Locate and identify every blood parasite.
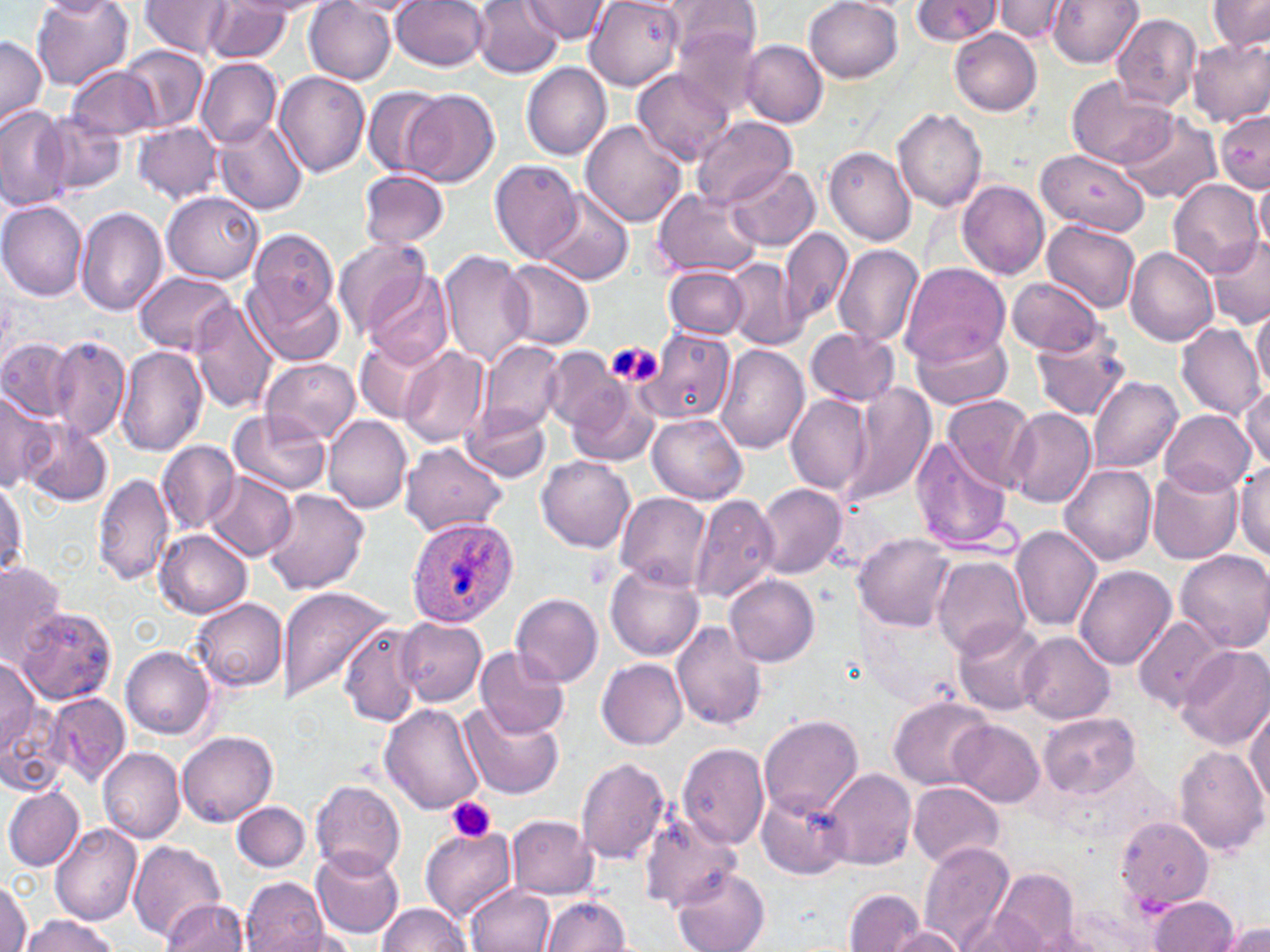

Approximate bounding boxes as [x1, y1, x2, y2] in pixels.
Plasmodium ovale-infected red blood cells: [406, 515, 518, 627].
No Plasmodium falciparum, Plasmodium malariae, Plasmodium vivax, Babesia divergens, or Trypanosoma brucei observed.

Platelet locations: [611, 343, 665, 388], [446, 796, 496, 844]. Uninfected red blood cell locations: [31, 0, 135, 91], [470, 0, 563, 77], [586, 0, 683, 89], [666, 0, 762, 67], [805, 0, 903, 82], [911, 0, 999, 44], [994, 0, 1072, 43], [1047, 0, 1143, 68], [1207, 0, 1270, 52], [138, 1, 233, 59], [330, 1, 425, 15], [393, 1, 491, 72], [520, 1, 611, 44], [305, 3, 397, 84], [202, 4, 295, 63], [1111, 14, 1202, 110], [672, 25, 767, 119], [949, 27, 1043, 117], [0, 35, 46, 129], [1189, 35, 1270, 126], [741, 41, 828, 127], [120, 46, 207, 133], [196, 58, 281, 149], [520, 62, 612, 161], [66, 66, 161, 142], [633, 68, 739, 166], [274, 69, 371, 176], [1065, 75, 1178, 169], [361, 86, 447, 178], [403, 89, 500, 187], [0, 105, 72, 211], [893, 108, 988, 212], [1214, 108, 1268, 193], [1118, 113, 1220, 204], [44, 116, 125, 193], [690, 117, 798, 207], [580, 118, 688, 228], [213, 119, 308, 215], [135, 123, 221, 203], [823, 145, 916, 246], [1035, 148, 1151, 236], [489, 160, 581, 263], [726, 162, 819, 251], [361, 168, 449, 251], [1252, 176, 1270, 255], [1167, 178, 1265, 279], [958, 180, 1051, 279], [652, 188, 761, 280], [162, 189, 262, 282], [537, 190, 633, 285], [0, 201, 87, 299], [75, 207, 167, 316], [1041, 219, 1141, 313], [247, 224, 340, 337], [780, 226, 851, 328], [1206, 235, 1269, 326], [334, 240, 436, 345], [834, 244, 925, 348], [1125, 246, 1218, 346], [439, 248, 533, 369], [501, 259, 594, 353], [724, 259, 802, 351], [901, 262, 1009, 366], [664, 266, 750, 339], [364, 269, 453, 369], [134, 271, 238, 355], [1006, 276, 1106, 358], [246, 279, 345, 369], [188, 296, 277, 415], [1251, 306, 1269, 394], [1175, 322, 1266, 420], [909, 326, 1016, 411], [806, 327, 899, 408], [1031, 329, 1133, 421], [634, 332, 737, 434], [47, 337, 131, 441], [355, 337, 445, 426], [1, 338, 78, 421], [478, 339, 564, 435], [715, 344, 810, 454], [117, 346, 209, 457], [398, 346, 490, 448], [541, 347, 621, 434], [261, 358, 360, 445], [1089, 376, 1184, 472], [564, 378, 660, 468], [1241, 382, 1270, 470], [838, 384, 938, 509], [0, 387, 55, 490], [785, 394, 875, 498], [943, 394, 1038, 492], [462, 402, 551, 483], [1005, 408, 1096, 507], [228, 409, 328, 497], [1160, 410, 1254, 498], [648, 413, 748, 505], [322, 415, 413, 515], [20, 418, 113, 508], [910, 437, 1016, 554], [155, 439, 239, 534], [399, 441, 508, 538], [537, 455, 636, 552], [1236, 463, 1270, 563], [1059, 464, 1157, 565], [1147, 465, 1244, 564], [92, 471, 176, 585], [206, 472, 296, 561], [0, 481, 28, 579], [755, 483, 847, 579], [262, 488, 371, 595], [615, 490, 711, 591], [689, 491, 780, 604], [1011, 525, 1103, 633], [155, 529, 253, 618], [854, 532, 957, 630], [1175, 551, 1270, 652], [931, 555, 1032, 658], [0, 560, 69, 661], [605, 565, 705, 661], [1074, 566, 1175, 669], [724, 575, 820, 667], [278, 585, 396, 707], [510, 592, 603, 688], [189, 597, 290, 693], [14, 608, 119, 706], [1134, 615, 1226, 713], [395, 617, 486, 705], [953, 619, 1047, 716], [339, 622, 427, 726], [672, 622, 768, 731], [1017, 632, 1116, 723], [476, 645, 570, 740], [1177, 645, 1270, 751], [119, 646, 216, 740], [0, 655, 44, 766], [597, 659, 688, 749], [1, 689, 68, 799], [43, 692, 131, 787], [887, 695, 993, 790], [460, 700, 566, 800], [1245, 702, 1269, 812], [379, 705, 485, 815], [1039, 711, 1140, 798], [761, 715, 864, 820], [950, 720, 1043, 807], [178, 731, 278, 827], [677, 743, 769, 851], [1171, 744, 1267, 855], [98, 747, 184, 844], [575, 758, 673, 865], [825, 768, 915, 869], [310, 780, 405, 878], [909, 781, 1004, 868], [4, 786, 85, 872], [758, 790, 849, 880], [233, 802, 310, 872], [639, 810, 742, 912], [507, 815, 598, 898], [1117, 816, 1215, 910], [50, 824, 142, 926], [419, 826, 515, 926], [130, 840, 228, 941], [919, 842, 1012, 950], [312, 847, 404, 942], [671, 866, 771, 952], [992, 869, 1082, 949], [0, 877, 32, 952], [240, 877, 330, 952], [466, 883, 555, 952], [845, 889, 925, 952], [542, 896, 632, 951], [1148, 896, 1240, 951], [158, 899, 251, 951], [377, 902, 474, 952], [957, 910, 1052, 951], [19, 913, 119, 952], [1216, 921, 1270, 952], [884, 927, 969, 951]. Slide-level diagnosis: Plasmodium ovale. Single field of view. Thin blood film. May-Grünwald-Giemsa stain. Image is 1270×952 pixels. 1000x magnification. Light microscopy.